Classify the preparation.
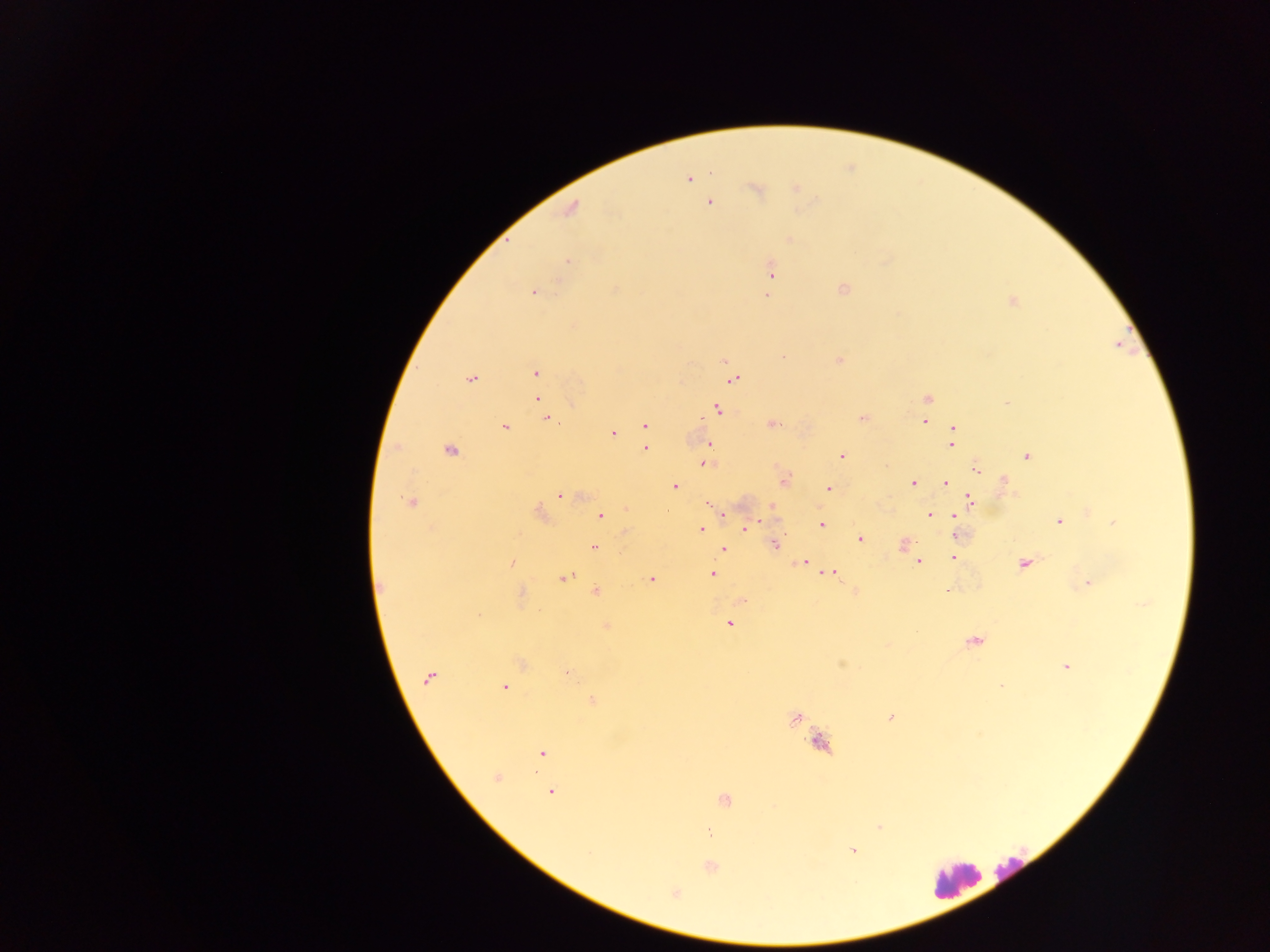
Thick blood film.

Approximate centers as {x, y} in pixels. Leukocyte locations: {820, 742}, {1012, 868}, {955, 878}. Plasmodium parasite locations: {689, 178}, {796, 189}, {756, 190}, {709, 202}, {571, 208}, {789, 238}, {567, 261}, {770, 270}, {842, 289}, {533, 291}, {766, 295}, {1012, 300}, {724, 360}, {838, 360}, {535, 373}, {734, 378}, {470, 379}, {537, 383}, {537, 399}, {926, 399}, {1007, 403}, {543, 409}, {717, 409}, {547, 417}, {862, 417}, {924, 422}, {645, 424}, {772, 424}, {504, 427}, {954, 428}, {612, 433}, {952, 435}, {644, 443}, {709, 443}, {951, 443}, {645, 448}, {450, 449}, {842, 455}, {1027, 455}, {705, 463}, {975, 468}, {783, 479}, {1003, 481}, {913, 482}, {945, 483}, {673, 486}, {828, 488}, {561, 494}, {970, 501}, {412, 502}, {708, 502}, {772, 505}, {538, 513}, {723, 513}, {600, 515}, {930, 515}, {954, 515}, {1058, 521}, {1114, 522}, {821, 525}, {744, 527}, {700, 530}, {624, 534}, {957, 534}, {859, 538}, {903, 543}, {774, 544}, {594, 547}, {722, 549}, {953, 557}, {919, 560}, {511, 563}, {804, 563}, {1024, 563}, {831, 572}, {712, 573}, {564, 577}, {651, 579}, {1087, 582}, {381, 588}, {596, 591}, {854, 591}, {948, 591}, {520, 595}, {741, 600}, {729, 623}, {605, 626}, {973, 640}, {840, 662}, {521, 663}, {1066, 666}, {566, 673}, {429, 677}, {1000, 685}, {504, 686}, {592, 701}, {890, 717}, {795, 718}, {542, 753}, {495, 778}, {550, 791}, {724, 799}, {878, 827}, {709, 833}, {853, 851}, {710, 867}, {675, 893}. One field of view. Collected in Ghana. Image is 1270×952 pixels. Mobile-phone photograph taken through the microscope.